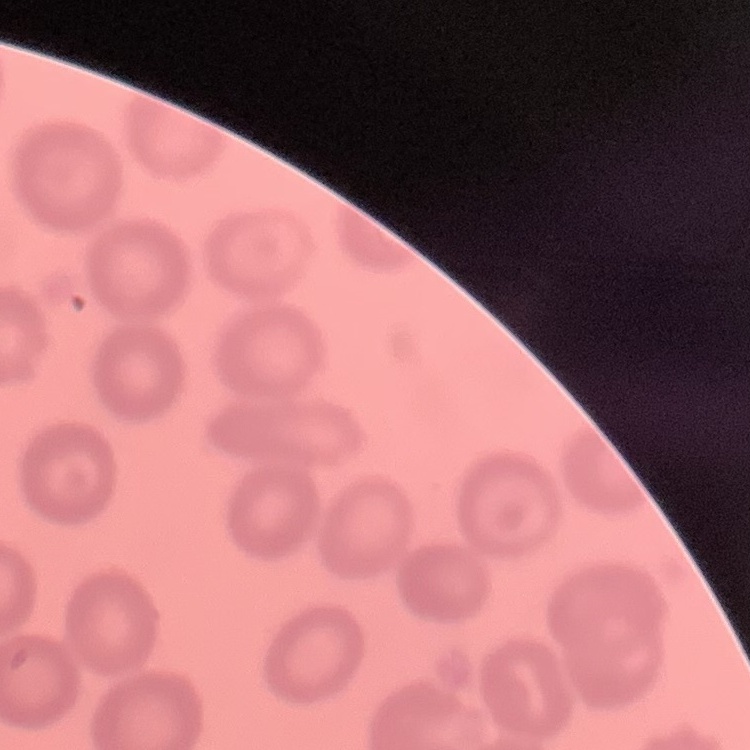

The red blood cells show no rouleaux formation. Thin peripheral smear. Square crop of a larger photomicrograph. Field's or Giemsa stain.